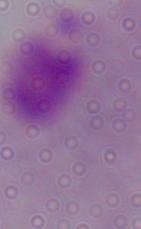

Photomicrograph. Captured at 1000x magnification. A trichomonad is seen.